Outline Plasmodium falciparum parasites and classify them by life-cycle stage.
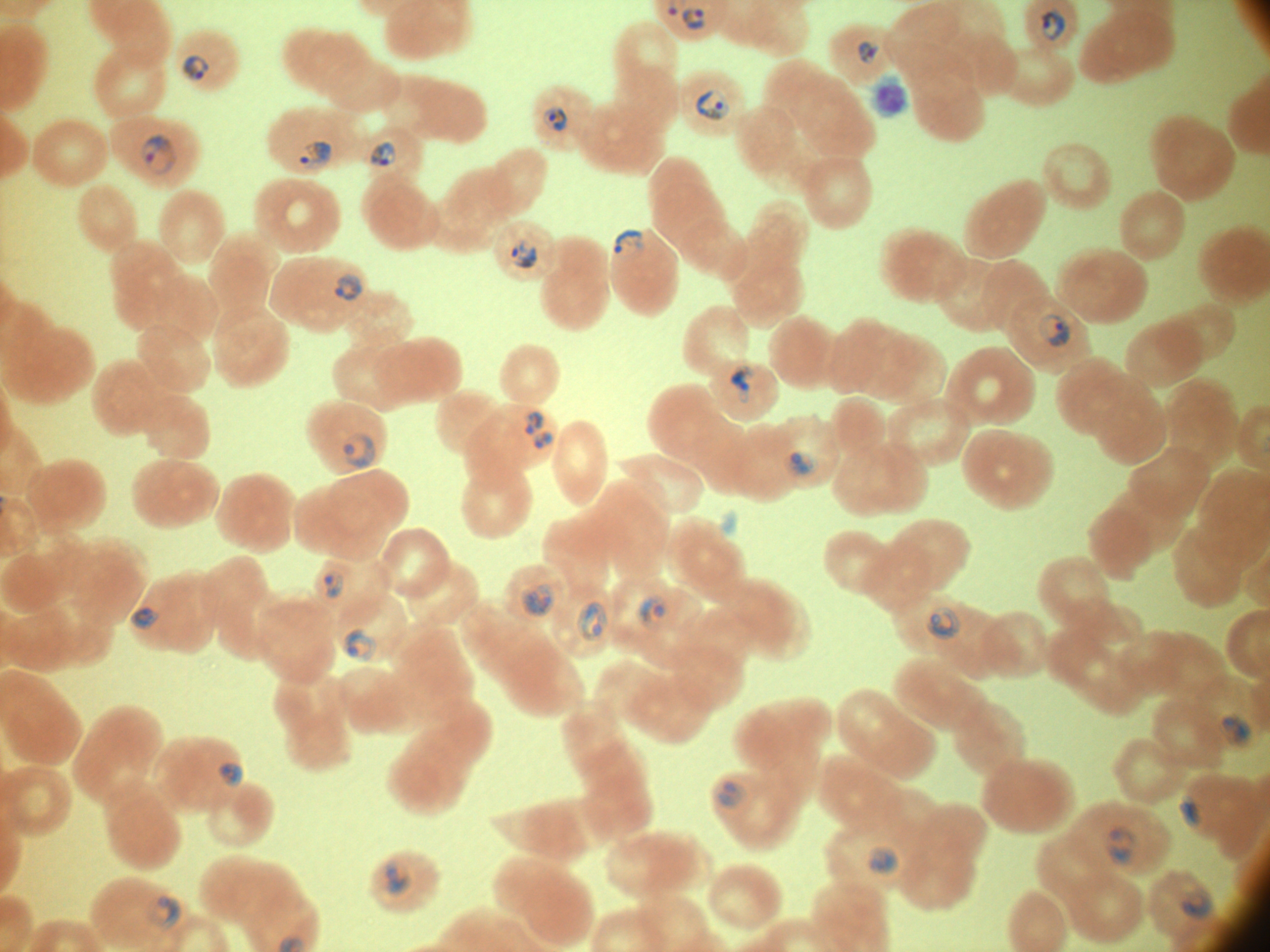
Approximate bounding boxes as [x1, y1, x2, y2] in pixels, from the source annotation, which is not necessarily exhaustive.
Ring forms: [682, 6, 707, 31], [1041, 6, 1067, 43], [857, 39, 880, 65], [183, 54, 210, 81], [696, 88, 731, 121], [543, 103, 568, 133], [141, 134, 178, 175], [300, 141, 332, 170], [369, 141, 396, 168], [613, 228, 643, 260], [510, 239, 538, 269], [334, 273, 363, 302], [1038, 314, 1070, 347], [731, 363, 757, 404], [523, 410, 545, 436], [530, 428, 555, 451], [342, 433, 376, 468], [782, 451, 820, 477], [323, 568, 345, 599], [520, 583, 555, 619], [635, 594, 670, 630], [576, 600, 608, 642], [130, 607, 162, 629], [925, 607, 961, 642], [342, 627, 377, 662], [1220, 713, 1253, 749], [217, 762, 244, 789], [715, 780, 747, 811], [1178, 794, 1202, 829], [1104, 824, 1138, 866], [865, 846, 900, 878], [385, 861, 411, 897], [1182, 886, 1214, 921], [147, 896, 181, 928].

Thin blood film. Acquired with a Leica DM2000 optical microscope and its built-in camera. Species: Plasmodium falciparum. Captured at 100x magnification. Image is 1270×952 pixels. Giemsa-stained preparation. One field from this slide.